Comment on the morphology of the red blood cells.
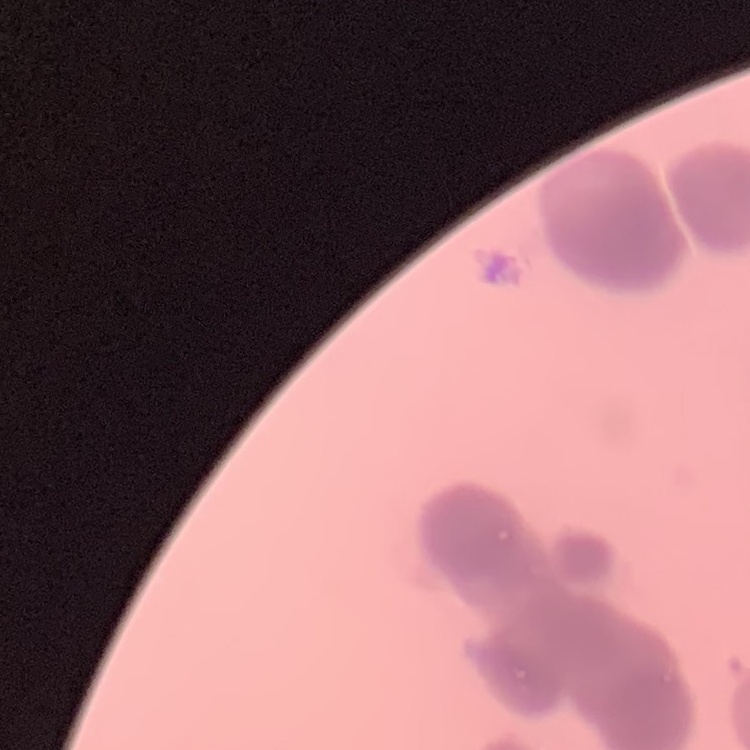

Rouleaux formation.

preparation = thin blood film
stain = Field's or Giemsa
image type = square crop of a larger photomicrograph